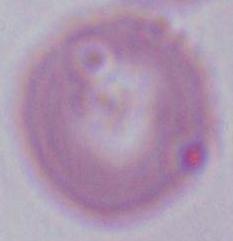

modality = micrograph
identification = red blood cell
magnification = 1000x